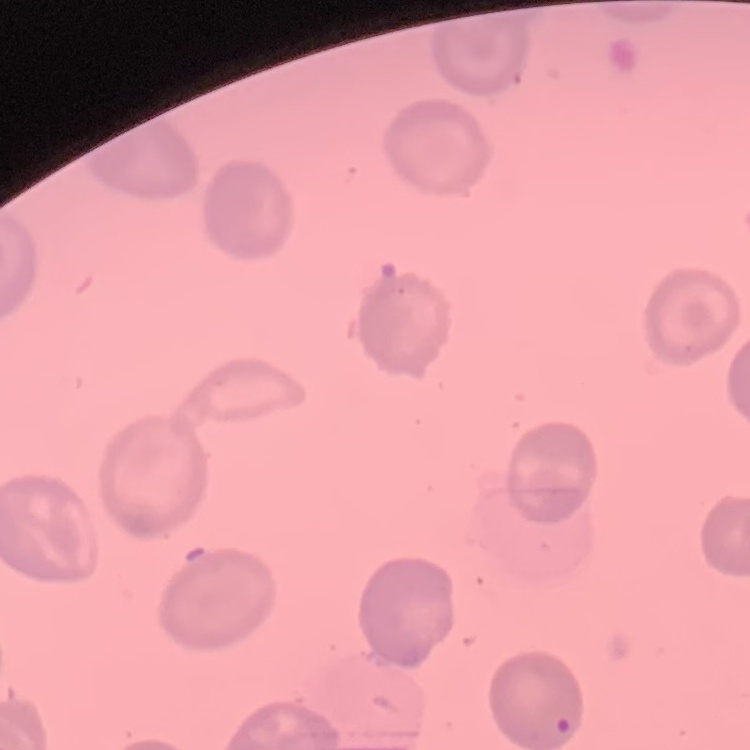

Summary:
  - Red blood cell morphology: no rouleaux formation
  - Image type: square crop of a larger photomicrograph
  - Stain: Field's or Giemsa
  - Preparation: thin peripheral smear